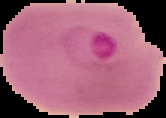
Summary:
  - Preparation: thin blood film
  - Result: malaria parasites detected
  - Image type: cell region segmented out of the field of view; surrounding area masked to black
  - Image size: 166×118 pixels